Assess this cell for malaria.
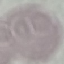

It is uninfected.

{
  "preparation": "thin blood film",
  "image_type": "automatically extracted cell patch, resized to 64 × 64 pixels",
  "capture": "smartphone camera at the microscope eyepiece",
  "stain": "Giemsa"
}